Report the malaria status of this cell.
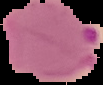

It is parasitized.

From a thin blood film. The area outside the segmented cell region is set to black. Image is 103×85 pixels.